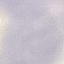
Summary:
  - Result: no malaria parasites detected
  - Capture: smartphone through the microscope eyepiece
  - Preparation: thin blood film
  - Image type: automatically extracted cell patch, resized to 64 × 64 pixels
  - Stain: Giemsa